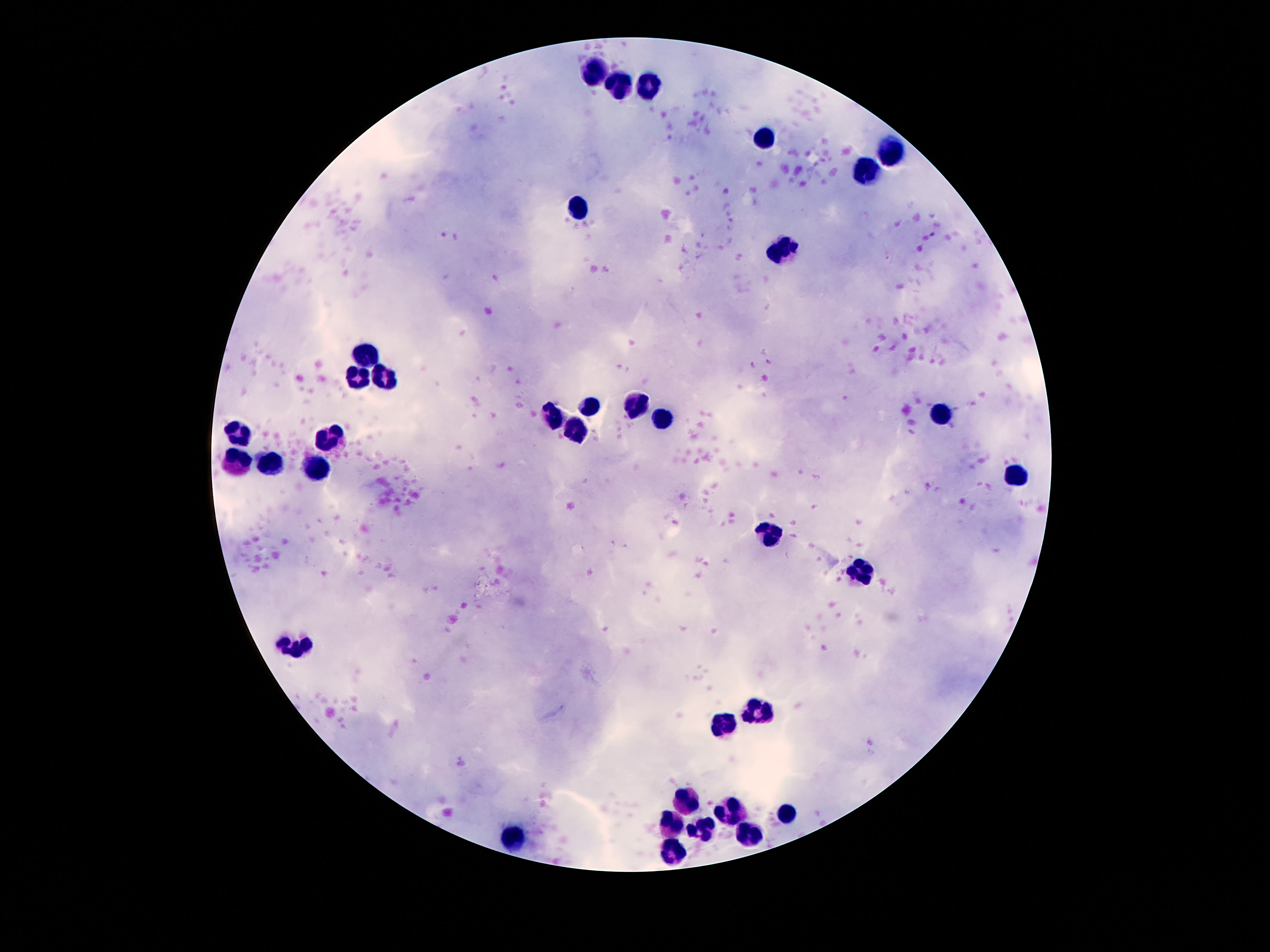
patient_malaria_status: negative
preparation: thick peripheral-blood smear
magnification: 100x
image_size: 1270×952 pixels
capture: smartphone camera through the microscope eyepiece
field_of_view: single
leukocyte_locations: 'approximate centers as (x, y) in pixels: (597, 75), (621, 86), (651, 86), (767, 141), (891, 153), (865, 174), (576, 205), (782, 250), (368, 354), (359, 376), (385, 377), (586, 406), (637, 409), (940, 414), (550, 417), (663, 419), (579, 433), (235, 436), (327, 437), (270, 465), (238, 466), (319, 468), (1015, 475), (768, 536), (861, 574), (299, 645), (754, 707), (723, 725), (688, 803), (733, 812), (781, 812), (674, 823), (704, 831), (749, 834), (516, 842), (676, 852)'
stain: Giemsa